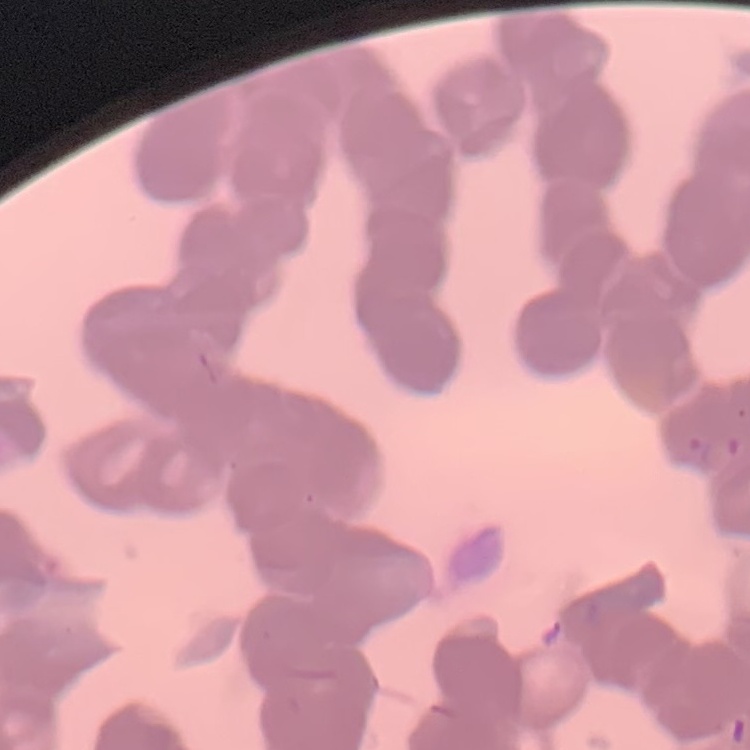

red blood cell morphology = rouleaux formation
image type = square crop of a larger photomicrograph
stain = Field's or Giemsa
preparation = thin peripheral smear